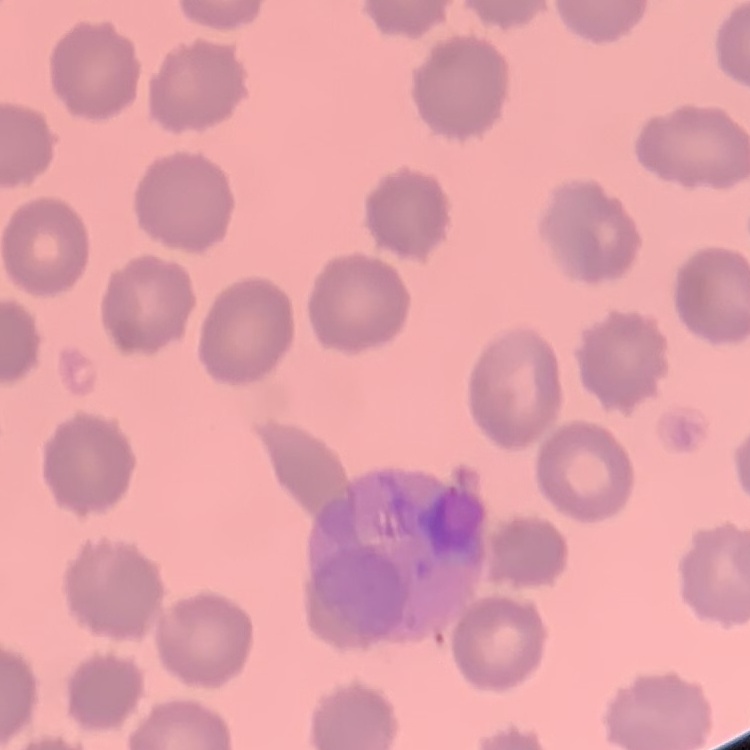
Summary:
  - Red blood cell morphology: no rouleaux formation
  - Preparation: thin blood film
  - Stain: Field's or Giemsa
  - Image type: square crop of a larger photomicrograph